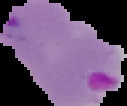 Image is 127×106 pixels. The area outside the segmented cell region is set to black. Malaria status: parasitized. From a thin blood film.